Report the malaria status of this cell.
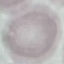

Uninfected.

Summary:
  - Capture: smartphone camera at the microscope eyepiece
  - Preparation: thin smear
  - Stain: Giemsa
  - Image type: automatically extracted cell patch, resized to 64 × 64 pixels